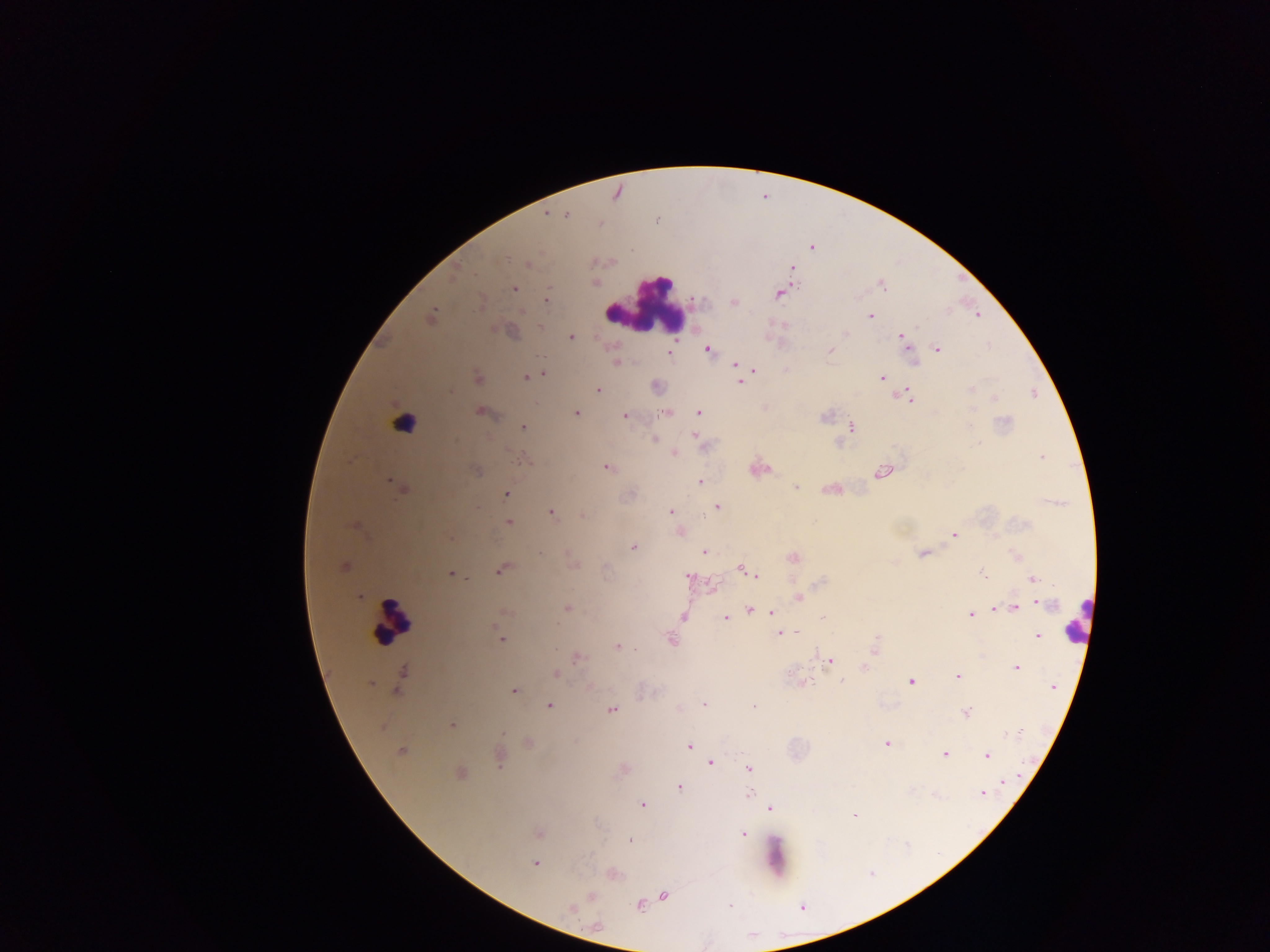

Approximate centers as x y in pixels. Malaria parasite locations: 567 215; 600 226; 526 265; 595 282; 514 289; 779 295; 734 303; 480 304; 522 310; 868 314; 977 314; 845 333; 900 336; 572 337; 708 349; 938 350; 829 351; 615 361; 734 362; 752 368; 542 374; 477 376; 526 377; 882 377; 740 383; 597 390; 971 390; 451 391; 901 395; 995 399; 972 408; 479 410; 669 412; 699 412; 575 413; 624 417; 972 423; 522 426; 851 426; 694 434; 654 439; 975 444; 674 453; 1041 457; 523 461; 607 467; 758 470; 880 471; 389 481; 701 482; 797 487; 506 495; 718 504; 672 512; 550 513; 584 517; 509 521; 678 533; 955 535; 632 548; 703 550; 922 553; 741 567; 748 571; 497 572; 982 572; 451 574; 757 574; 689 576; 1034 579; 710 586; 798 598; 1041 601; 567 608; 994 608; 1014 608; 750 610; 773 613; 972 615; 685 616; 725 617; 822 617; 782 632; 795 632; 1037 636; 671 639; 501 641; 616 646; 637 649; 577 656; 829 662; 865 667; 1018 669; 557 675; 402 676; 958 678; 911 681; 371 685; 513 691; 704 704; 549 705; 754 706; 611 709; 965 713; 452 725; 502 734; 885 743; 689 747; 402 752; 945 755; 989 756; 711 762; 750 768; 1009 781; 678 787; 750 794; 981 794; 642 804; 770 808; 854 816; 741 833; 629 839; 535 864; 664 895; 638 904; 571 908. Leukocyte locations: 648 307; 385 616; 1071 628. Sample from Ghana. Image is 1270×952 pixels. Mobile-phone photograph taken through the microscope. Single field of view. Thick blood film.